Assess this cell for malaria.
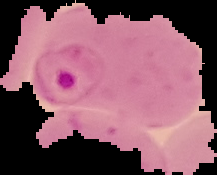

Parasitized.

Summary:
  - Image size: 217×175 pixels
  - Preparation: thin blood smear
  - Image type: segmented cell region on a black background